Comment on the morphology of the red blood cells.
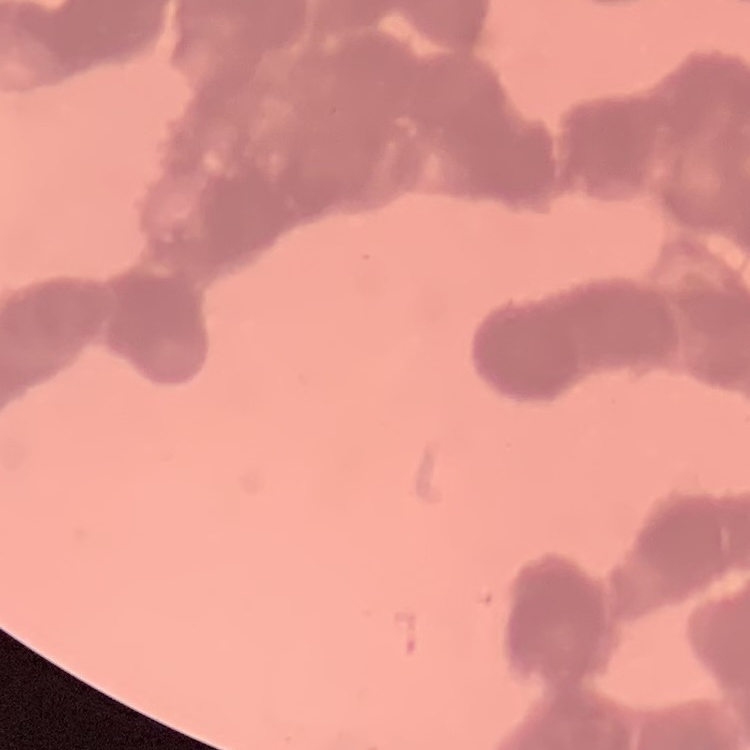
Rouleaux formation.

Summary:
  - Image type: one tile cut from a larger photomicrograph
  - Stain: Field's or Giemsa
  - Preparation: thin blood smear